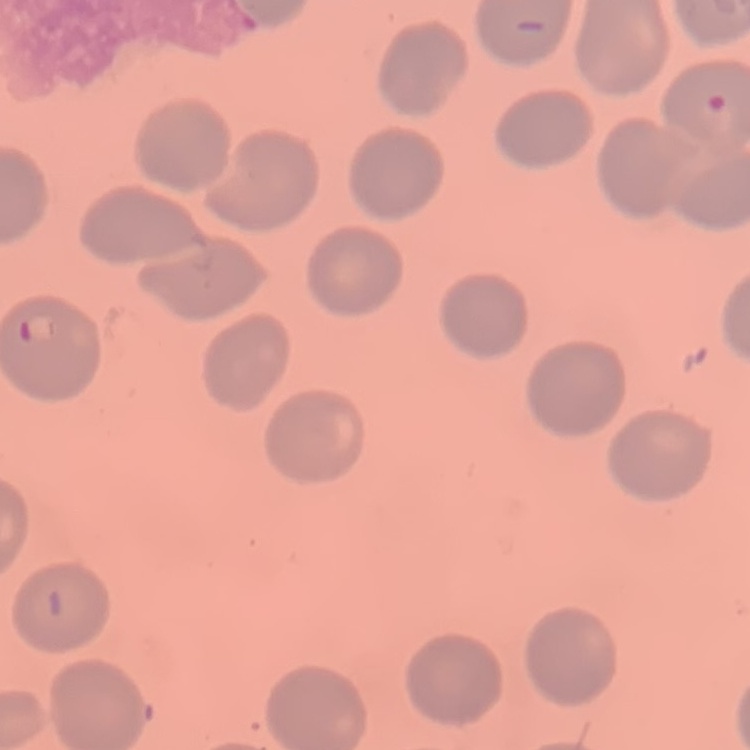

red blood cell morphology = no rouleaux formation
preparation = thin peripheral smear
stain = Field's or Giemsa
image type = square crop of a larger photomicrograph